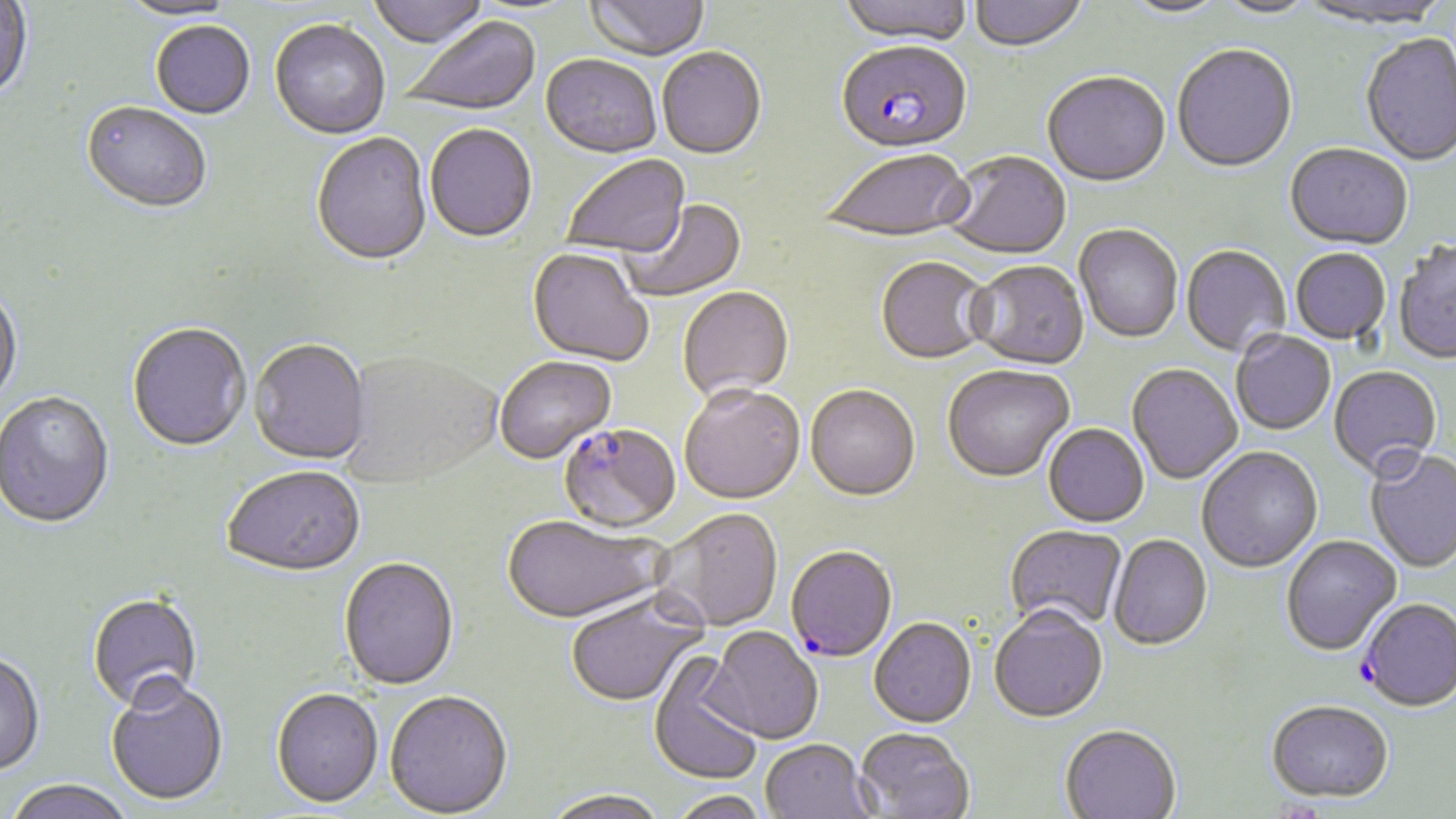
Approximate bounding boxes as (x1, y1, x2, y2) in pixels. Plasmodium falciparum-infected red blood cell locations: (836, 44, 972, 156), (558, 424, 681, 536), (785, 548, 897, 664), (1359, 600, 1456, 714). Uninfected red blood cell locations: (368, 0, 490, 51), (587, 0, 710, 64), (838, 0, 974, 48), (969, 0, 1088, 54), (1121, 0, 1227, 20), (0, 1, 34, 104), (117, 1, 243, 24), (1213, 1, 1317, 20), (1295, 1, 1452, 32), (402, 17, 542, 118), (269, 21, 390, 142), (151, 23, 255, 121), (1360, 35, 1456, 168), (1172, 46, 1298, 175), (657, 49, 766, 162), (540, 56, 661, 160), (1043, 73, 1170, 189), (80, 104, 212, 216), (425, 126, 537, 245), (312, 134, 432, 269), (1284, 145, 1413, 252), (821, 151, 974, 245), (942, 152, 1071, 262), (562, 156, 691, 262), (622, 200, 748, 303), (1074, 226, 1183, 345), (1392, 243, 1456, 366), (1181, 246, 1290, 358), (1291, 249, 1391, 346), (526, 250, 653, 369), (875, 259, 993, 366), (967, 262, 1090, 371), (0, 287, 24, 412), (678, 288, 794, 403), (127, 324, 251, 454), (1231, 332, 1336, 436), (249, 341, 370, 467), (340, 353, 502, 490), (495, 357, 617, 465), (1127, 365, 1242, 485), (942, 367, 1074, 485), (1328, 367, 1442, 482), (805, 387, 920, 504), (679, 388, 806, 507), (0, 392, 115, 531), (1043, 425, 1149, 529), (1197, 448, 1323, 574), (1364, 451, 1456, 575), (223, 469, 366, 579), (654, 510, 783, 634), (502, 518, 666, 627), (1005, 526, 1127, 634), (1108, 536, 1212, 653), (1282, 537, 1402, 658), (338, 559, 459, 692), (86, 592, 204, 714), (566, 595, 708, 709), (989, 610, 1108, 726), (869, 620, 977, 730), (703, 628, 823, 745), (0, 652, 45, 777), (648, 656, 764, 786), (105, 679, 229, 806), (271, 690, 384, 811), (385, 692, 513, 818), (1266, 704, 1394, 805), (1060, 727, 1181, 819), (854, 730, 974, 819), (760, 741, 876, 818), (4, 780, 136, 819), (541, 791, 671, 819), (668, 791, 773, 819). Slide-level diagnosis: Plasmodium falciparum. Image is 1456×819 pixels. Captured at 1000x magnification. Thin blood film. Optical microscopy. May-Grünwald-Giemsa-stained preparation. Single field of view.